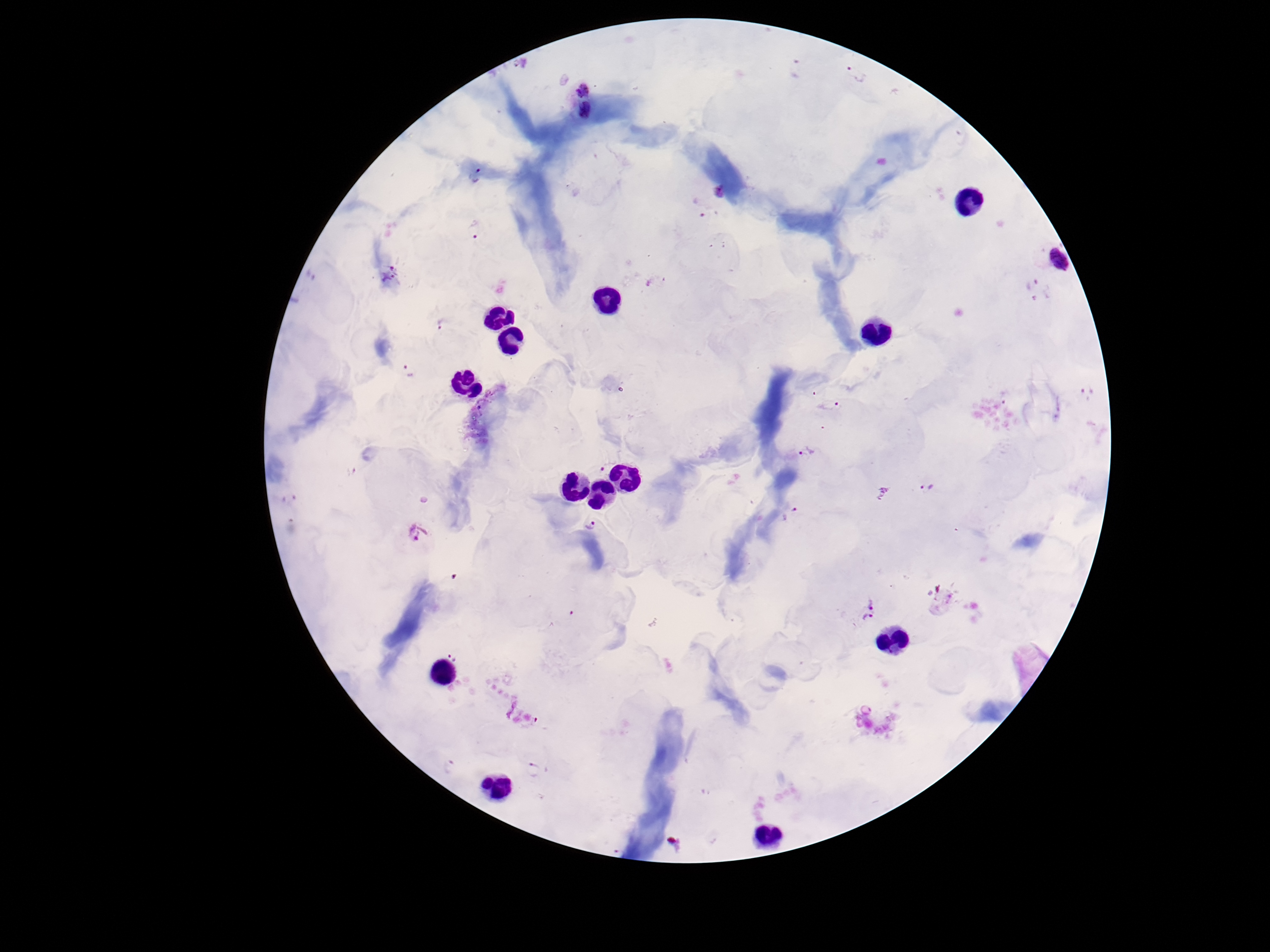
Plasmodium parasite locations = approximate centers as {x, y} in pixels: {795, 69}, {855, 74}, {581, 92}, {584, 110}, {475, 176}, {719, 191}, {474, 229}, {1049, 257}, {387, 274}, {1032, 284}, {440, 323}, {408, 371}, {1087, 392}, {829, 405}, {806, 452}, {603, 464}, {926, 489}, {791, 512}, {591, 526}, {418, 534}, {871, 603}, {869, 620}, {865, 711}, {450, 766}, {537, 771}
stain = Giemsa
magnification = 100x
patient malaria status = positive
field of view = one from this slide
image size = 1270×952 pixels
capture = smartphone camera through the microscope eyepiece
preparation = thick blood smear